Give the extent of all Plasmodium falciparum-infected red blood cells.
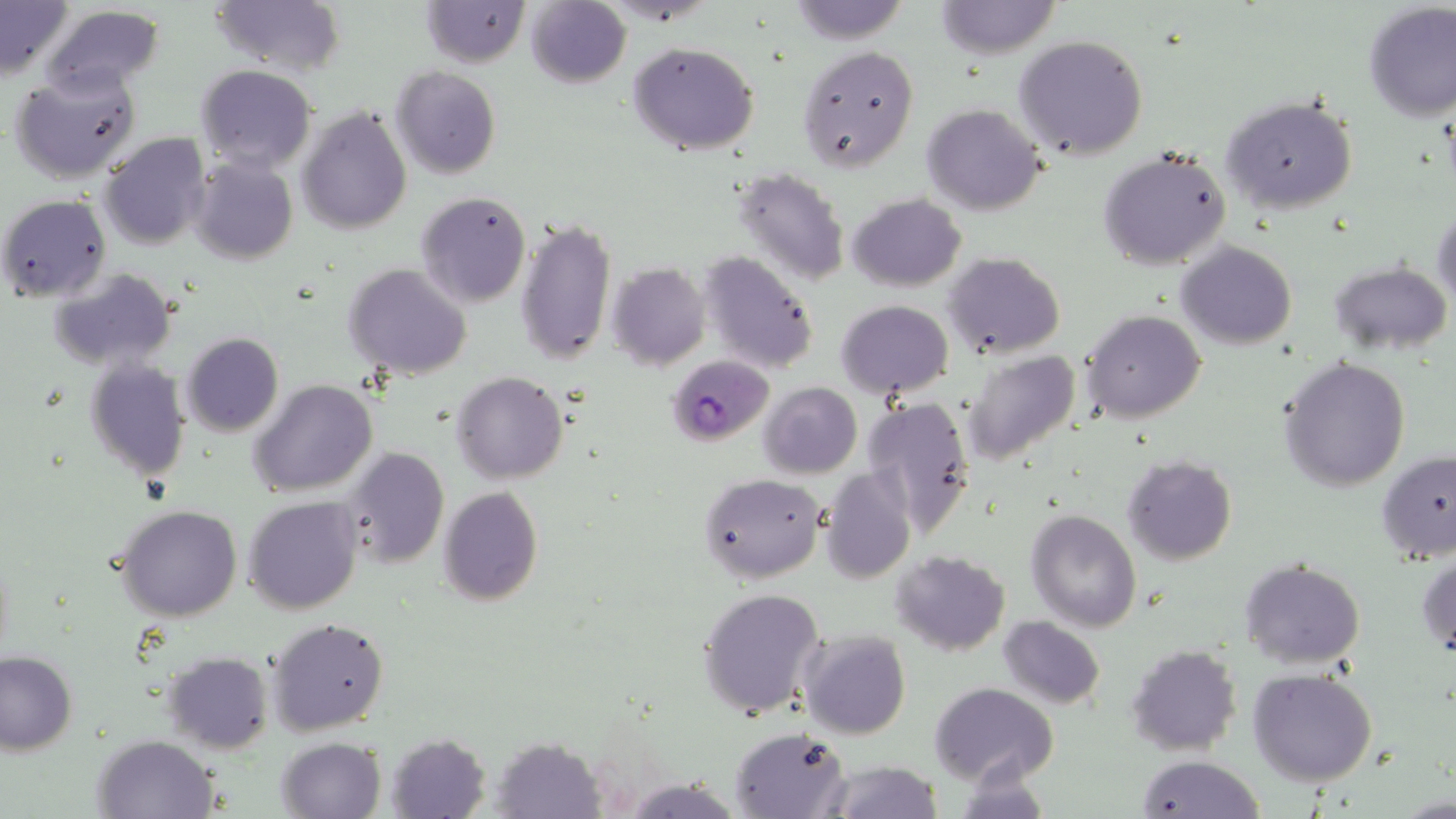

Approximate bounding boxes as (x1, y1, x2, y2) in pixels.
Plasmodium falciparum-infected red blood cells: (666, 354, 773, 445).

Summary:
  - Uninfected red blood cell locations: (210, 0, 345, 75), (421, 0, 530, 67), (935, 0, 1060, 59), (0, 1, 75, 79), (525, 1, 630, 88), (787, 1, 912, 45), (1363, 2, 1456, 122), (39, 4, 166, 99), (1013, 34, 1148, 159), (628, 42, 760, 156), (799, 46, 919, 171), (197, 64, 316, 173), (391, 66, 500, 178), (9, 67, 144, 184), (1221, 94, 1359, 213), (923, 103, 1044, 215), (297, 107, 411, 233), (100, 133, 211, 249), (1098, 148, 1231, 270), (189, 157, 297, 264), (730, 166, 851, 287), (415, 191, 531, 308), (847, 193, 966, 292), (2, 194, 111, 300), (1433, 207, 1456, 307), (516, 215, 616, 367), (1177, 241, 1296, 350), (696, 251, 820, 374), (944, 252, 1065, 358), (1329, 259, 1451, 355), (608, 262, 710, 369), (343, 263, 472, 381), (52, 268, 176, 370), (835, 300, 954, 399), (1081, 310, 1204, 424), (180, 333, 283, 437), (964, 351, 1083, 467), (1278, 356, 1410, 492), (84, 359, 191, 482), (452, 372, 568, 484), (250, 379, 377, 497), (758, 382, 862, 478), (861, 395, 977, 534), (340, 447, 449, 569), (1377, 449, 1456, 561), (1121, 455, 1236, 566), (821, 469, 916, 583), (698, 472, 827, 586), (438, 486, 544, 606), (243, 496, 364, 614), (115, 504, 242, 622), (1026, 508, 1142, 631), (891, 549, 1010, 656), (1417, 549, 1456, 661), (1239, 560, 1366, 668), (697, 587, 825, 721), (269, 616, 389, 736), (997, 616, 1106, 710), (799, 629, 912, 740), (1125, 644, 1242, 754), (0, 648, 77, 755), (163, 651, 271, 753), (1248, 670, 1377, 788), (929, 683, 1058, 787), (731, 726, 850, 818), (385, 732, 490, 818), (94, 735, 217, 818), (492, 735, 606, 817), (277, 737, 386, 819), (1135, 755, 1265, 817), (824, 761, 945, 818)
  - Slide-level diagnosis: Plasmodium falciparum
  - Modality: optical microscopy
  - Image size: 1456×819 pixels
  - Preparation: thin blood smear
  - Magnification: 1000x
  - Field of view: one of a larger specimen
  - Stain: May-Grünwald-Giemsa